Assess this cell for malaria.
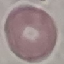
Uninfected.

image_type: cell patch, automatically extracted from a larger field of view and resized to 64 × 64 pixels
capture: smartphone through the microscope eyepiece
stain: Giemsa
preparation: thin blood film